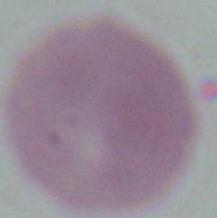
Summary:
  - Modality: micrograph
  - Magnification: 1000x
  - Identification: erythrocyte